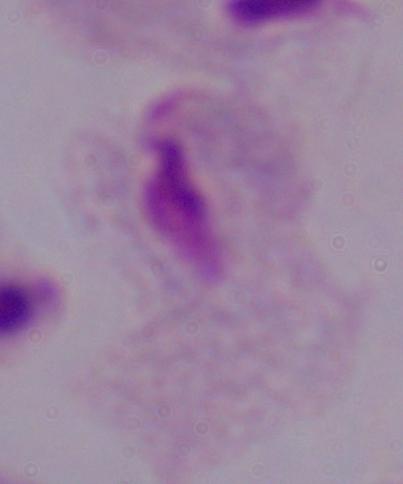

A trichomonad is shown. Photomicrograph. 1000x magnification.